Identify the preparation type.
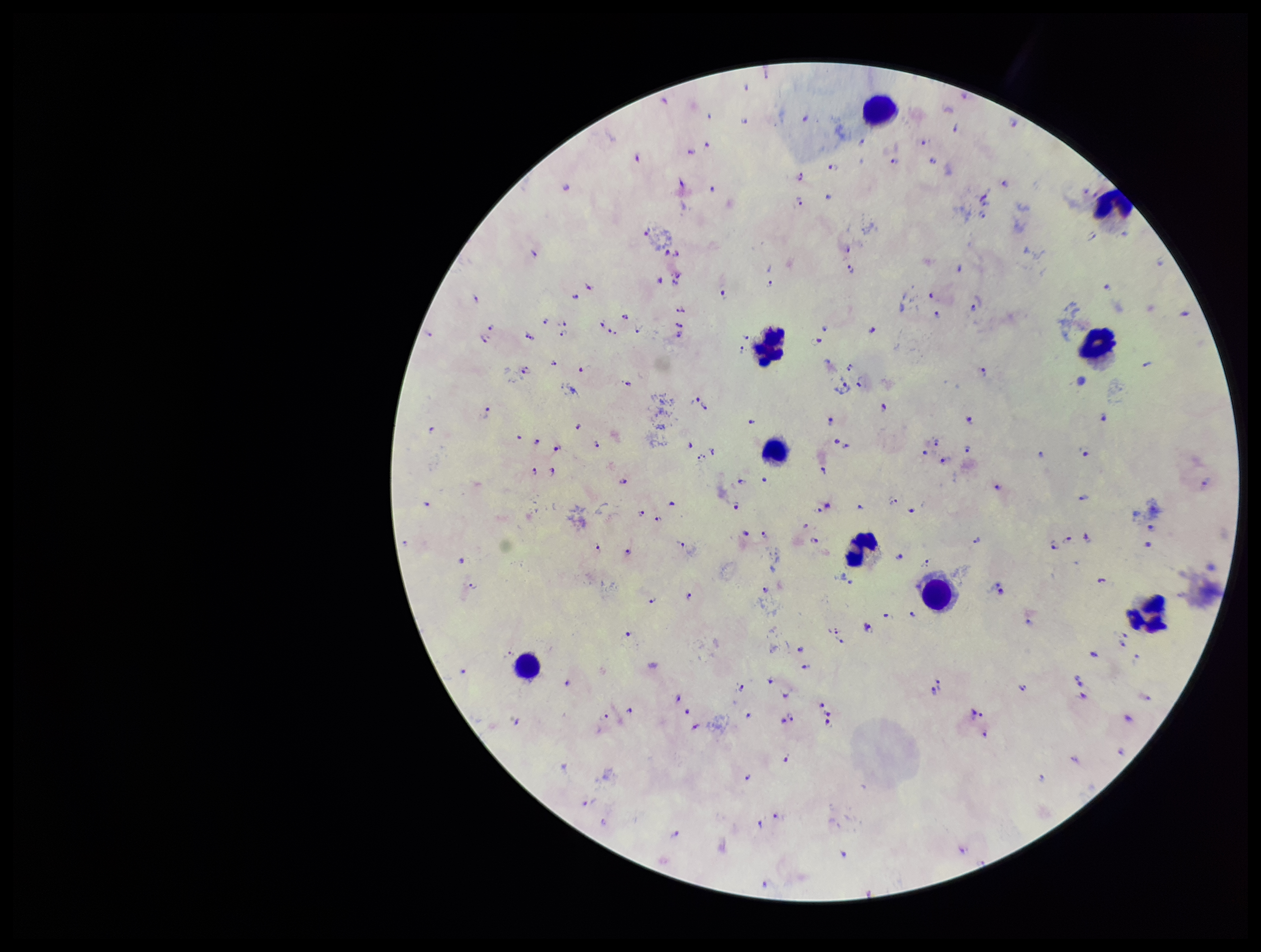
A thick smear.

Patient malaria status: infected. Plasmodium parasites: identified. Parasite count: 146. Photographed through the microscope eyepiece with a smartphone camera. One field from this slide. Image is 1261×952 pixels. Giemsa stain. Species reported for this patient: Plasmodium falciparum. Leukocyte count: 9.